Locate every malaria parasite.
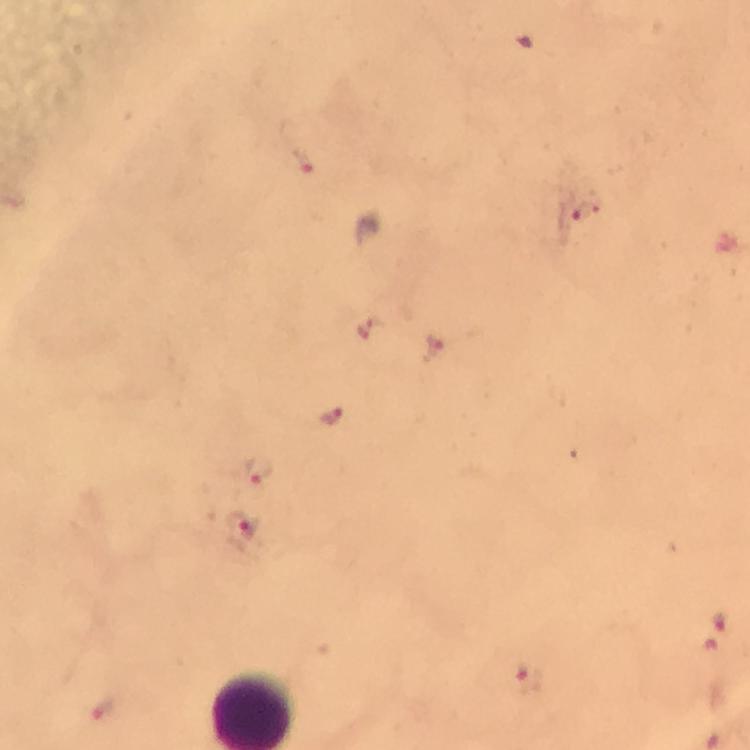

Approximate centers as {x, y} in pixels.
Malaria parasites: {303, 163}, {582, 212}, {373, 330}, {436, 348}, {329, 414}, {258, 469}, {240, 532}, {720, 622}, {529, 679}, {100, 710}.

Summary:
  - Stain: Giemsa
  - Cropped from: one field of view
  - Image size: 750×750 pixels
  - Magnification: 100x
  - Preparation: thick smear
  - Capture: smartphone camera through the microscope
  - Context: from a diagnostic examination for malaria
  - Immersion oil: applied